Report the malaria status of this cell.
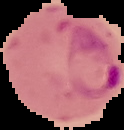

Parasitized.

From a thin blood film. Segmented cell region on a black background. Image is 124×130 pixels.